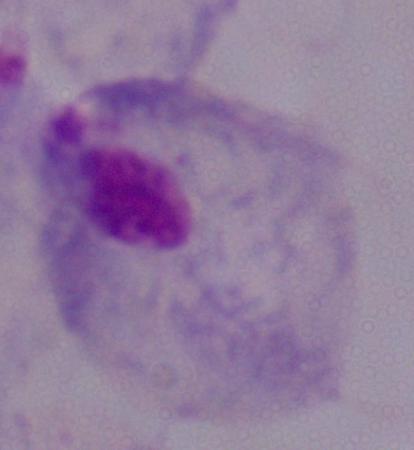
Captured at 1000x magnification. A trichomonad is seen. Photomicrograph.